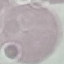 Malaria status: uninfected. Giemsa stain. Acquired by smartphone through the microscope eyepiece. Cell patch, automatically extracted from a larger field of view and resized to 64 × 64 pixels. Thin blood film.